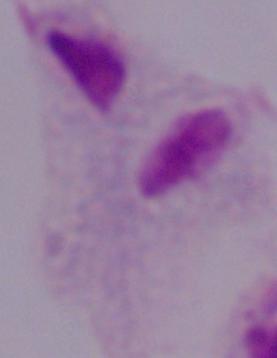

Micrograph. 1000x magnification. A trichomonad is seen.